Classify this cell by malaria status.
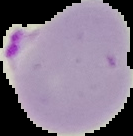
Parasitized.

{
  "image_type": "segmented cell region on a black background",
  "preparation": "thin blood smear",
  "image_size": "133×136 pixels"
}